Identify the preparation type.
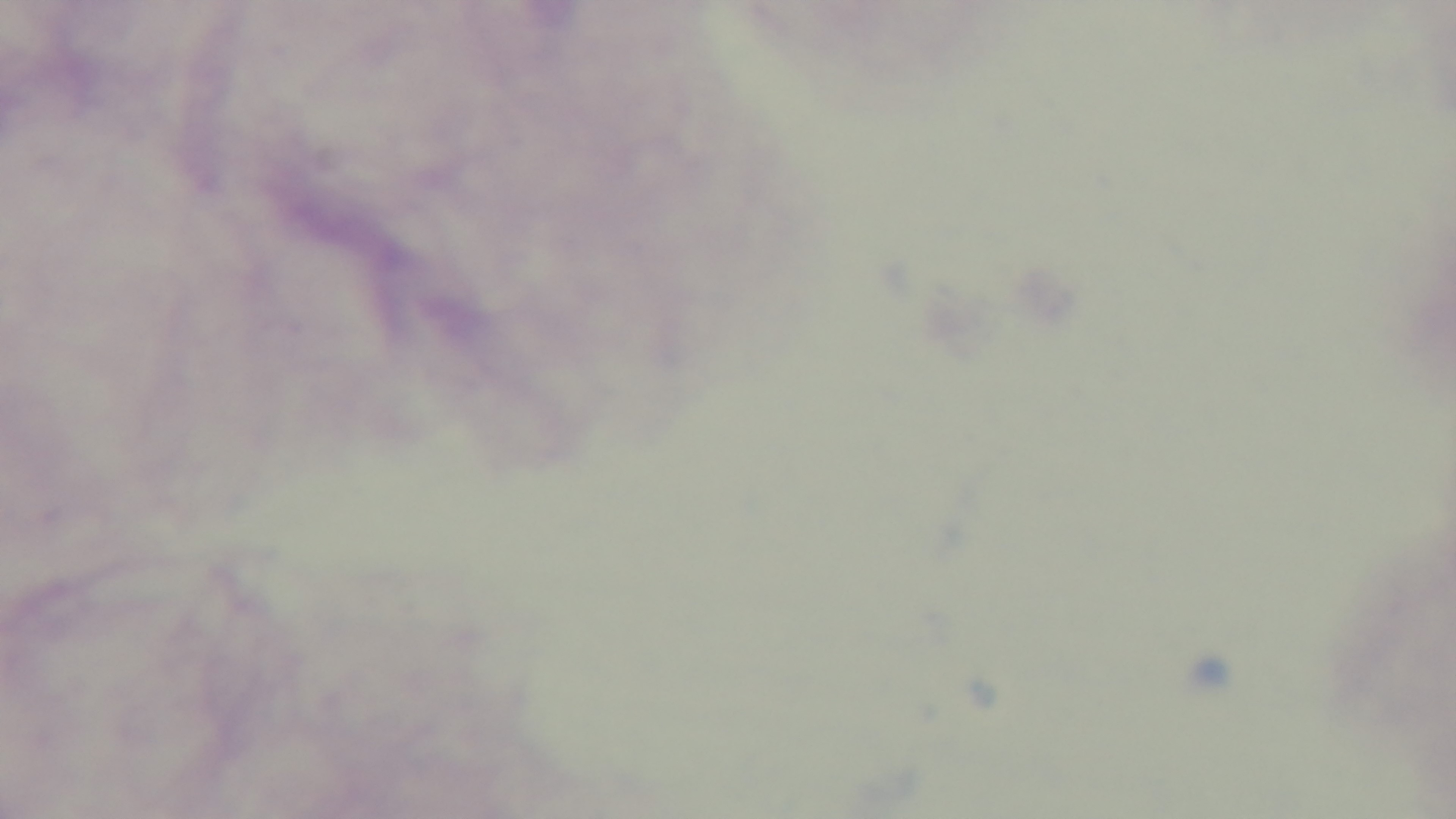

Thick.

malaria_status: uninfected
stain: Giemsa
field_of_view: single
objective: 100x oil immersion
modality: light microscopy
capture: mounted 4K digital camera